Give the extent of all Plasmodium falciparum-infected red blood cells.
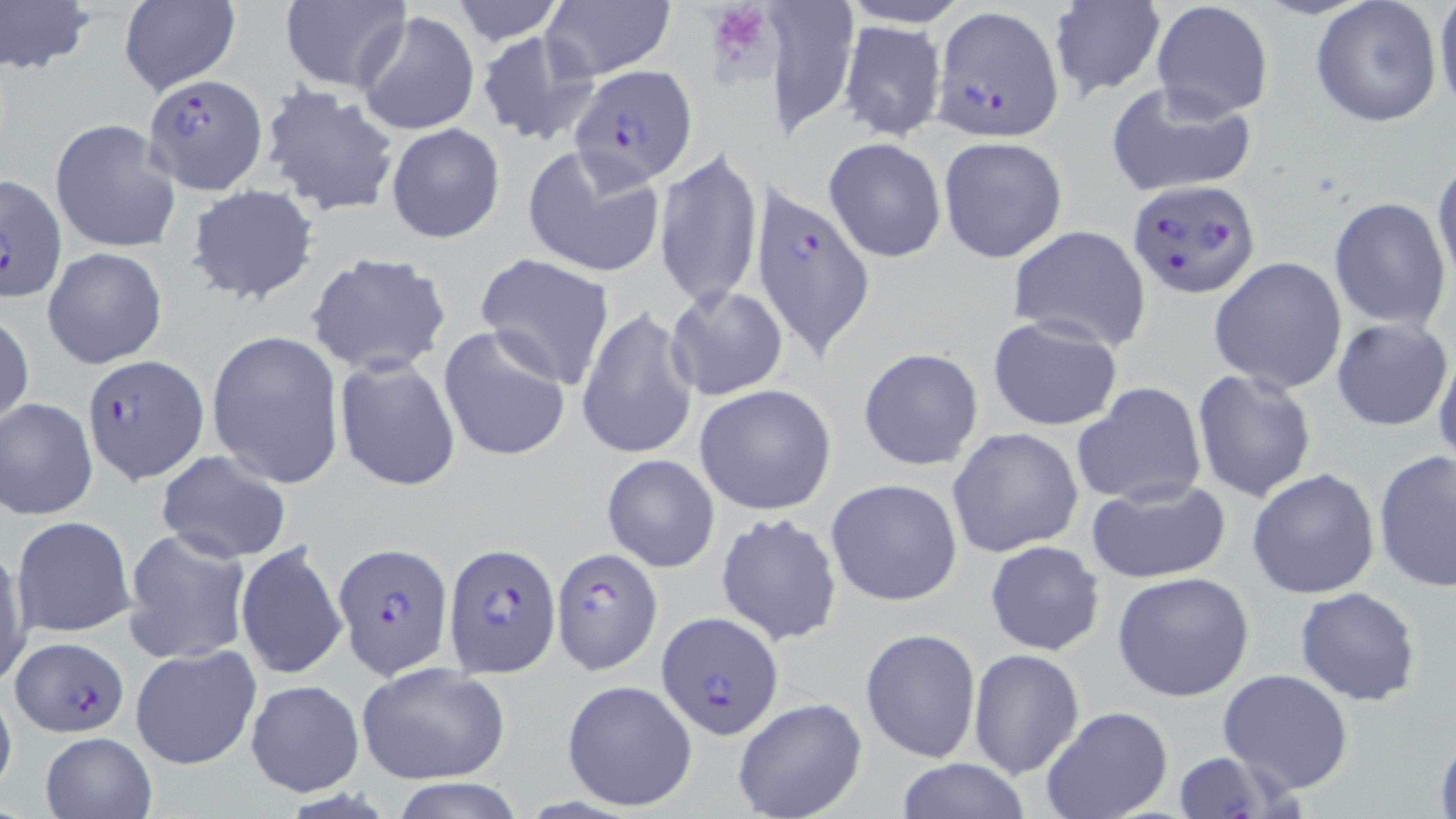
Approximate bounding boxes as [x1, y1, x2, y2] in pixels.
Plasmodium falciparum-infected red blood cells: [932, 6, 1065, 140], [571, 64, 700, 189], [142, 72, 270, 197], [0, 173, 67, 304], [1126, 178, 1258, 297], [750, 183, 877, 361], [81, 353, 207, 483], [332, 541, 452, 679], [443, 543, 559, 676], [551, 548, 662, 674], [654, 611, 785, 738], [9, 639, 130, 738].

Summary:
  - Uninfected red blood cell locations: [0, 0, 94, 79], [279, 0, 412, 92], [450, 0, 566, 44], [775, 0, 858, 140], [1308, 0, 1445, 126], [1435, 0, 1456, 121], [1047, 1, 1166, 99], [117, 2, 241, 96], [542, 2, 675, 82], [1151, 2, 1273, 119], [357, 10, 479, 136], [839, 20, 946, 140], [474, 30, 601, 146], [1105, 81, 1258, 200], [258, 85, 399, 219], [50, 118, 180, 254], [385, 123, 506, 243], [939, 135, 1069, 264], [824, 137, 946, 264], [655, 143, 763, 311], [520, 144, 666, 280], [1431, 158, 1455, 289], [186, 183, 319, 305], [1329, 196, 1452, 329], [1006, 226, 1154, 351], [43, 245, 168, 369], [304, 251, 452, 377], [475, 253, 617, 392], [1209, 256, 1347, 393], [664, 285, 787, 402], [577, 307, 701, 460], [0, 309, 34, 431], [986, 314, 1123, 431], [1332, 317, 1452, 431], [438, 324, 571, 463], [206, 328, 345, 489], [1433, 343, 1456, 470], [857, 347, 983, 471], [333, 357, 461, 492], [1191, 369, 1318, 504], [1071, 382, 1207, 508], [695, 384, 838, 516], [1, 397, 98, 521], [948, 427, 1084, 558], [1374, 449, 1455, 593], [156, 451, 292, 564], [602, 453, 720, 572], [1246, 466, 1380, 599], [826, 478, 965, 606], [1085, 479, 1230, 584], [715, 511, 842, 648], [13, 515, 135, 638], [123, 528, 249, 663], [235, 539, 348, 682], [985, 540, 1105, 655], [1, 543, 31, 688], [1112, 570, 1257, 703], [1294, 587, 1422, 706], [860, 627, 980, 763], [129, 643, 262, 771], [968, 649, 1085, 779], [356, 663, 510, 785], [1216, 668, 1354, 795], [245, 679, 362, 795], [560, 679, 698, 813], [0, 684, 17, 800], [732, 697, 868, 819], [1041, 707, 1171, 819], [1432, 726, 1455, 817], [39, 731, 156, 818], [1167, 750, 1289, 818], [895, 758, 1031, 819], [390, 778, 528, 818]
  - Platelet locations: [706, 2, 777, 78]
  - Slide-level diagnosis: Plasmodium falciparum
  - Preparation: thin blood film
  - Modality: light microscopy
  - Stain: May-Grünwald-Giemsa
  - Field of view: one of a larger specimen
  - Magnification: 1000x
  - Image size: 1456×819 pixels